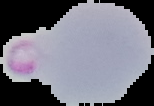
Summary:
  - Result: malaria parasites identified
  - Image size: 154×106 pixels
  - Preparation: thin blood smear
  - Image type: segmented cell region on a black background